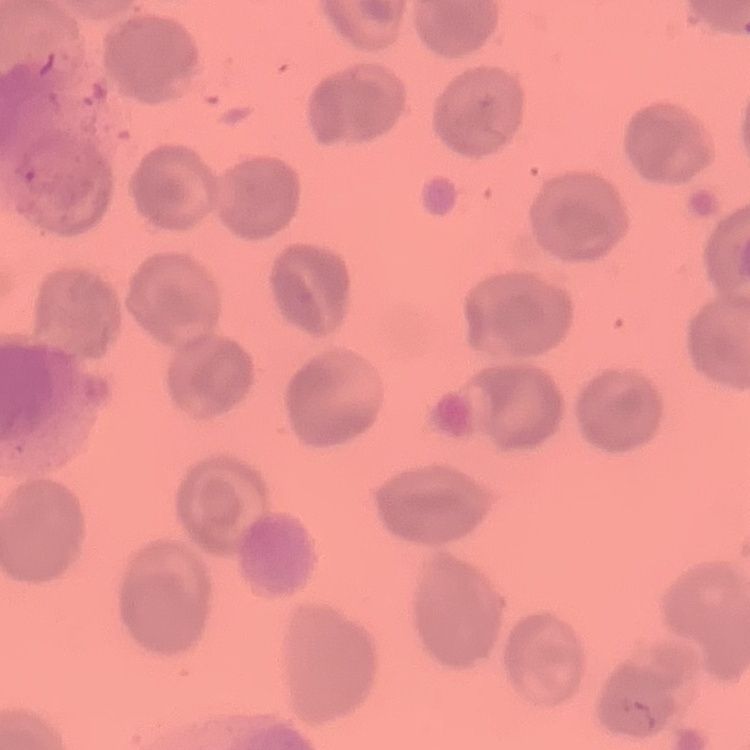

erythrocyte_morphology: no rouleaux formation
image_type: square crop of a larger photomicrograph
stain: Field's or Giemsa
preparation: thin blood film